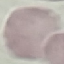
malaria_status: uninfected
image_type: cell patch, automatically extracted from a larger field of view and resized to 64 × 64 pixels
stain: Giemsa
preparation: thin blood smear
capture: smartphone camera at the microscope eyepiece